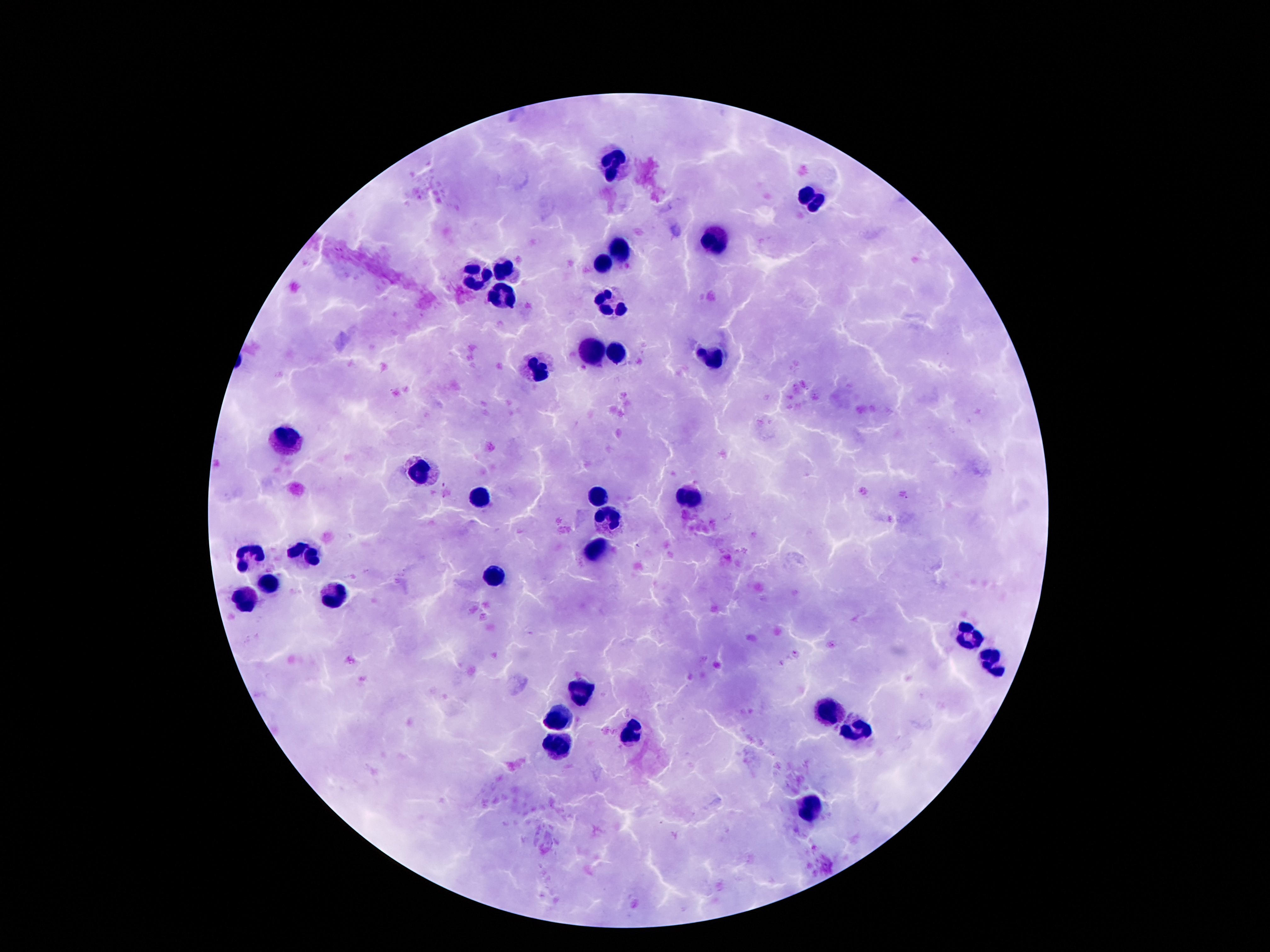
patient_malaria_status: uninfected
leukocyte_locations: 'approximate centers as [x, y] in pixels: [613, 163], [811, 198], [713, 240], [620, 249], [603, 263], [503, 266], [478, 272], [499, 297], [611, 303], [620, 350], [594, 352], [709, 357], [538, 371], [288, 433], [419, 472], [597, 496], [482, 497], [688, 497], [606, 520], [305, 550], [597, 553], [254, 556], [494, 577], [267, 583], [244, 597], [330, 597], [969, 632], [988, 662], [585, 688], [827, 712], [561, 720], [855, 728], [631, 734], [559, 744], [811, 808]'
capture: smartphone camera through the microscope eyepiece
preparation: thick peripheral-blood smear
image_size: 1270×952 pixels
magnification: 100x
field_of_view: one from this slide
stain: Giemsa